Locate and identify every blood parasite.
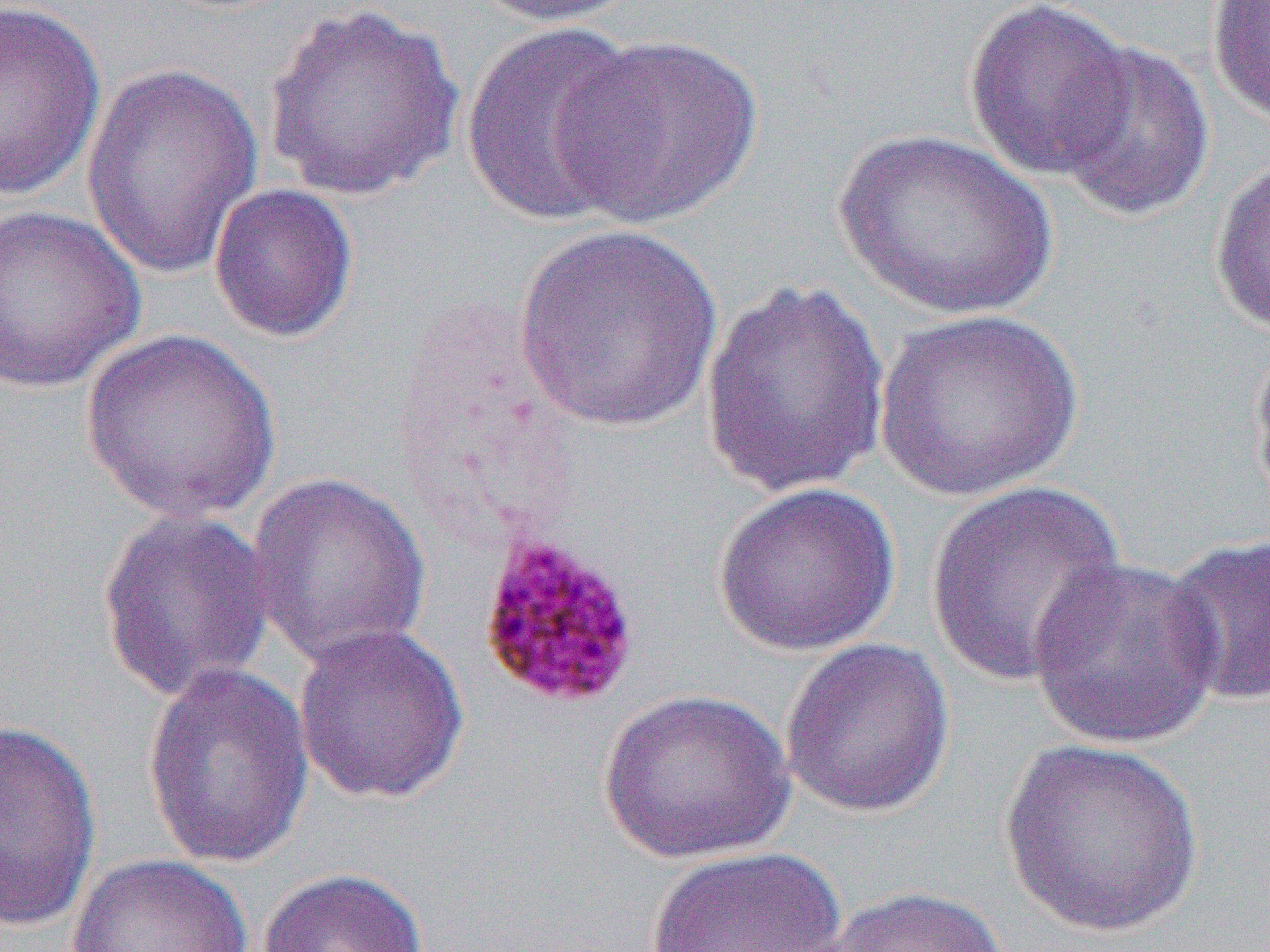
Approximate bounding boxes as [x1, y1, x2, y2] in pixels.
Plasmodium malariae-infected red blood cells: [475, 530, 644, 711].
No Plasmodium falciparum, Plasmodium ovale, Plasmodium vivax, Babesia divergens, or Trypanosoma brucei observed.

{
  "slide_level_diagnosis": "Plasmodium malariae",
  "magnification": "1000x",
  "image_size": "1270×952 pixels",
  "uninfected_red_blood_cell_locations": "approximate bounding boxes as [x1, y1, x2, y2] in pixels: [468, 0, 638, 28], [1206, 0, 1270, 124], [963, 1, 1136, 181], [0, 2, 106, 202], [261, 2, 466, 202], [461, 22, 649, 227], [551, 33, 764, 229], [1051, 39, 1215, 222], [81, 64, 264, 282], [832, 128, 1059, 322], [1207, 156, 1270, 338], [208, 183, 359, 344], [0, 204, 146, 395], [512, 223, 724, 433], [700, 278, 893, 500], [872, 308, 1085, 502], [80, 328, 281, 524], [1247, 328, 1270, 521], [245, 470, 433, 668], [923, 481, 1129, 690], [711, 482, 901, 657], [95, 507, 277, 704], [1162, 533, 1270, 708], [1026, 555, 1225, 750], [291, 622, 469, 805], [779, 638, 956, 819], [141, 659, 314, 870], [597, 689, 795, 864], [0, 718, 101, 933], [999, 737, 1204, 938], [644, 846, 848, 951], [66, 853, 254, 952], [256, 867, 430, 952], [816, 885, 1017, 952]",
  "preparation": "thin blood smear",
  "modality": "light microscopy",
  "field_of_view": "one of a larger specimen"
}